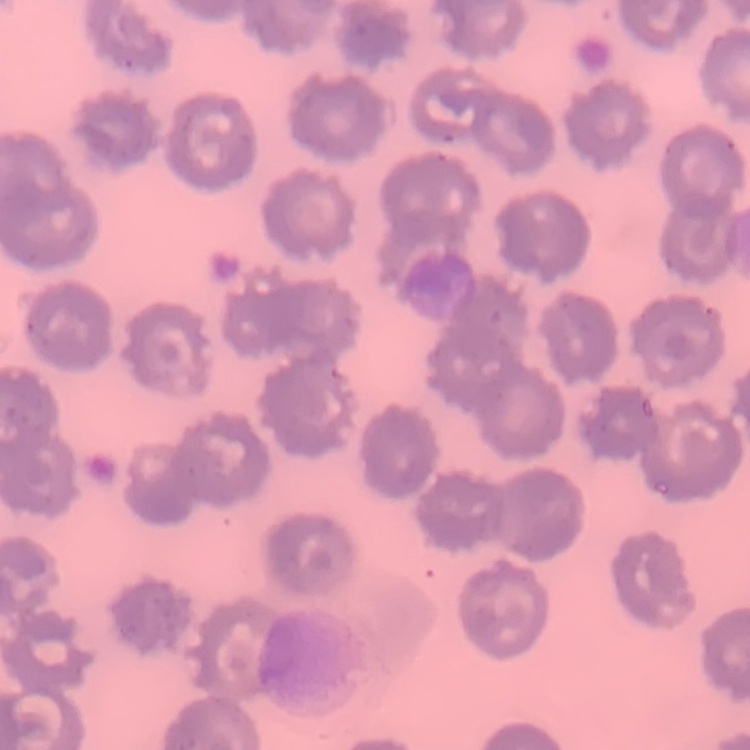 The red blood cells show no rouleaux formation. Field's or Giemsa stain. Thin blood film. One tile cut from a larger photomicrograph.